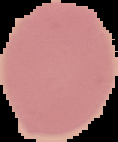 Cell region segmented out of the field of view; the surrounding area is masked to black. From a thin blood film. Result: no Plasmodium parasites seen. Image is 118×142 pixels.